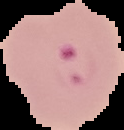
Summary:
  - Image size: 124×130 pixels
  - Result: Plasmodium parasites identified
  - Preparation: thin blood smear
  - Image type: segmented cell region on a black background